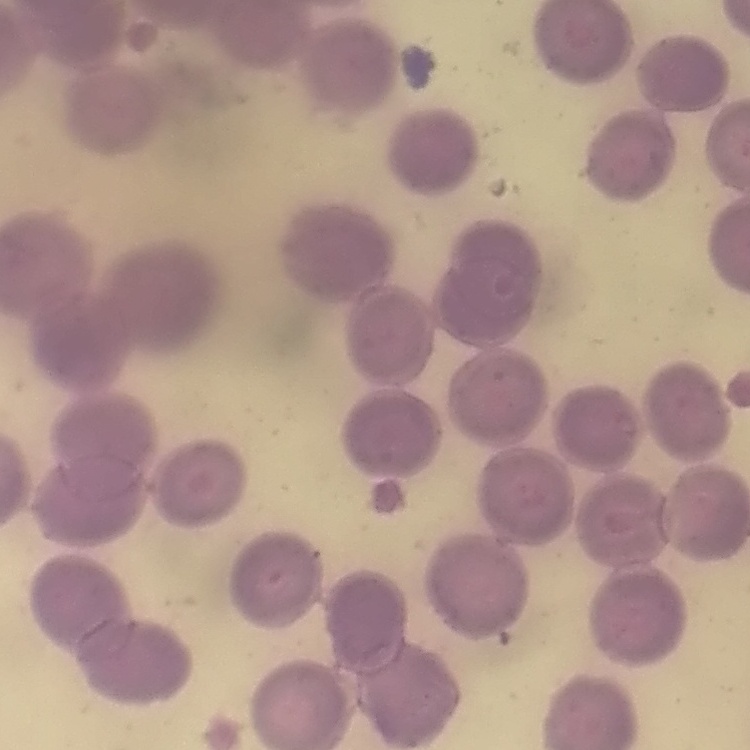
red_blood_cell_morphology: no rouleaux formation
stain: Field's or Giemsa
preparation: thin peripheral smear
image_type: one tile cut from a larger photomicrograph